Name the blood parasite species.
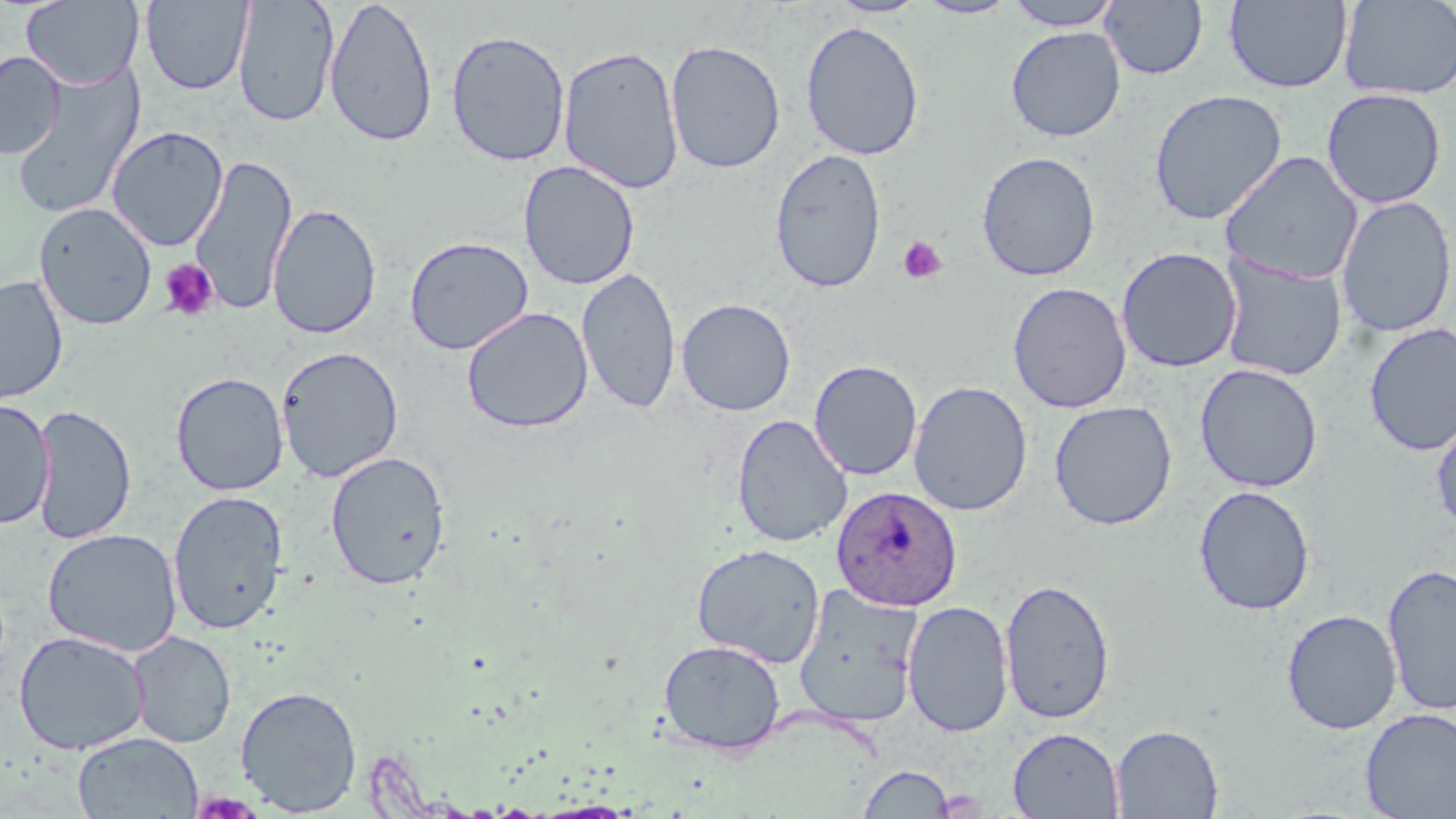
Plasmodium ovale.

preparation = thin blood smear
uninfected red blood cell locations = approximate bounding boxes as named x1/y1/x2/y2 corners in pixels: (x1=21, y1=0, x2=144, y2=89), (x1=141, y1=0, x2=254, y2=95), (x1=233, y1=0, x2=340, y2=127), (x1=324, y1=0, x2=438, y2=148), (x1=829, y1=0, x2=928, y2=18), (x1=916, y1=0, x2=1019, y2=19), (x1=1002, y1=0, x2=1124, y2=31), (x1=1100, y1=0, x2=1208, y2=79), (x1=1224, y1=0, x2=1353, y2=93), (x1=1339, y1=1, x2=1456, y2=100), (x1=800, y1=20, x2=925, y2=161), (x1=1005, y1=26, x2=1126, y2=142), (x1=445, y1=29, x2=571, y2=167), (x1=665, y1=38, x2=785, y2=174), (x1=558, y1=45, x2=685, y2=194), (x1=0, y1=51, x2=65, y2=159), (x1=9, y1=62, x2=146, y2=221), (x1=1321, y1=88, x2=1447, y2=209), (x1=1148, y1=89, x2=1288, y2=225), (x1=106, y1=126, x2=228, y2=252), (x1=770, y1=148, x2=887, y2=293), (x1=976, y1=151, x2=1101, y2=282), (x1=1220, y1=151, x2=1364, y2=285), (x1=189, y1=153, x2=297, y2=316), (x1=518, y1=160, x2=640, y2=290), (x1=1335, y1=195, x2=1456, y2=338), (x1=33, y1=202, x2=157, y2=330), (x1=268, y1=203, x2=382, y2=340), (x1=405, y1=235, x2=533, y2=355), (x1=1116, y1=246, x2=1242, y2=373), (x1=1218, y1=255, x2=1346, y2=381), (x1=577, y1=266, x2=681, y2=414), (x1=0, y1=275, x2=68, y2=405), (x1=1007, y1=281, x2=1132, y2=413), (x1=676, y1=298, x2=796, y2=416), (x1=461, y1=307, x2=594, y2=433), (x1=1363, y1=322, x2=1456, y2=457), (x1=276, y1=345, x2=405, y2=482), (x1=809, y1=359, x2=923, y2=481), (x1=1194, y1=363, x2=1323, y2=493), (x1=171, y1=372, x2=289, y2=496), (x1=908, y1=380, x2=1033, y2=516), (x1=0, y1=399, x2=55, y2=530), (x1=1049, y1=400, x2=1177, y2=530), (x1=31, y1=404, x2=137, y2=545), (x1=1431, y1=408, x2=1456, y2=537), (x1=732, y1=413, x2=853, y2=547), (x1=325, y1=451, x2=451, y2=590), (x1=1194, y1=485, x2=1316, y2=615), (x1=168, y1=489, x2=288, y2=635), (x1=42, y1=528, x2=183, y2=657), (x1=691, y1=543, x2=826, y2=667), (x1=1381, y1=561, x2=1456, y2=717), (x1=998, y1=577, x2=1116, y2=723), (x1=792, y1=586, x2=924, y2=729), (x1=902, y1=600, x2=1014, y2=737), (x1=1281, y1=608, x2=1402, y2=735), (x1=14, y1=630, x2=149, y2=755), (x1=128, y1=631, x2=236, y2=748), (x1=658, y1=638, x2=786, y2=756), (x1=235, y1=684, x2=363, y2=815), (x1=1360, y1=707, x2=1456, y2=818), (x1=1111, y1=723, x2=1225, y2=818), (x1=1008, y1=727, x2=1124, y2=818), (x1=72, y1=732, x2=203, y2=818), (x1=858, y1=763, x2=955, y2=818)
image size = 1456×819 pixels
field of view = one of a larger specimen
platelet locations = approximate bounding boxes as named x1/y1/x2/y2 corners in pixels: (x1=897, y1=236, x2=947, y2=284), (x1=159, y1=258, x2=220, y2=322)
stain = May-Grünwald-Giemsa
Plasmodium ovale-infected red blood cell locations = approximate bounding boxes as named x1/y1/x2/y2 corners in pixels: (x1=830, y1=484, x2=963, y2=612)
magnification = 1000x
modality = light microscopy